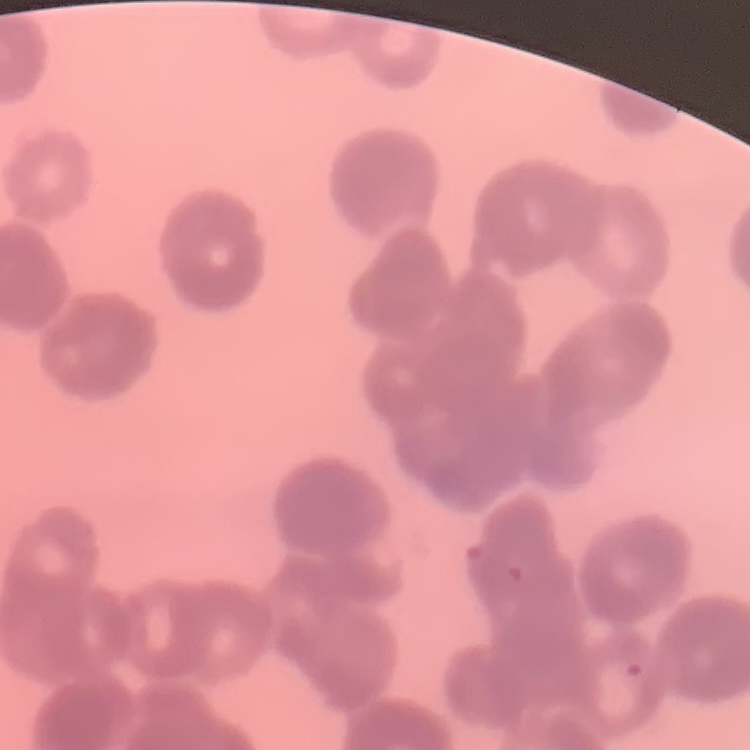
erythrocyte_morphology: rouleaux formation
stain: Field's or Giemsa
image_type: square crop of a larger photomicrograph
preparation: thin blood smear